Report the malaria status of this cell.
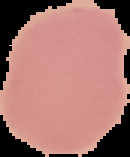
It is uninfected.

{
  "image_type": "segmented cell region with the area outside set to black",
  "preparation": "thin blood smear",
  "image_size": "130×157 pixels"
}